Identify the parasite.
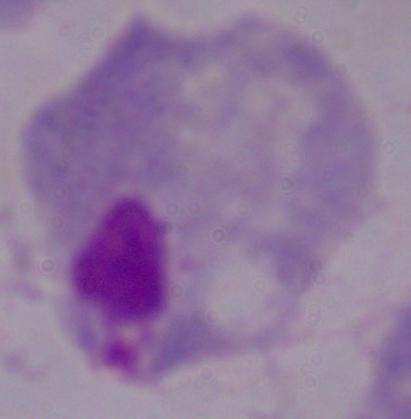

A trichomonad.

Summary:
  - Modality: photomicrograph
  - Magnification: 1000x